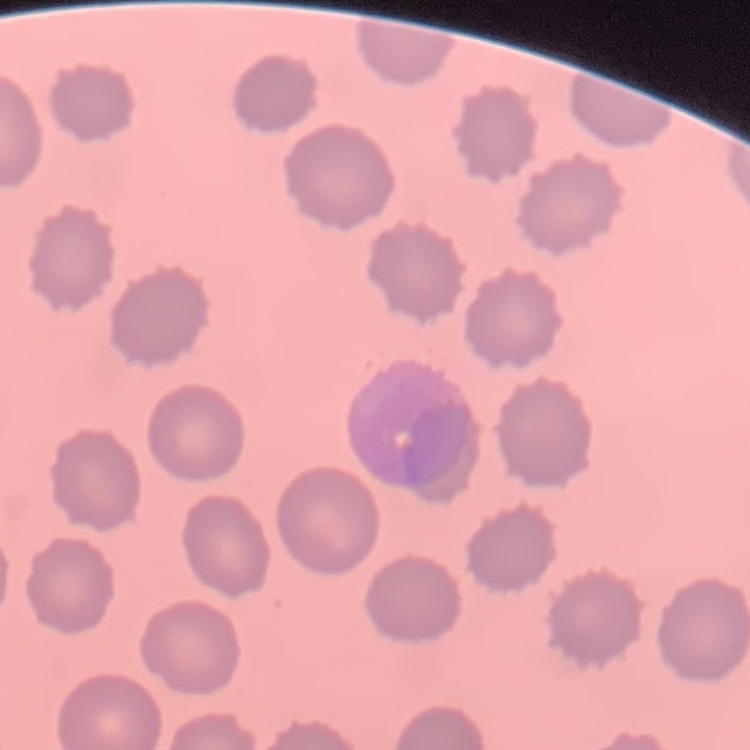

The erythrocytes show no rouleaux formation. Field's or Giemsa stain. Thin peripheral smear. Square crop of a larger photomicrograph.